Locate and identify every blood parasite.
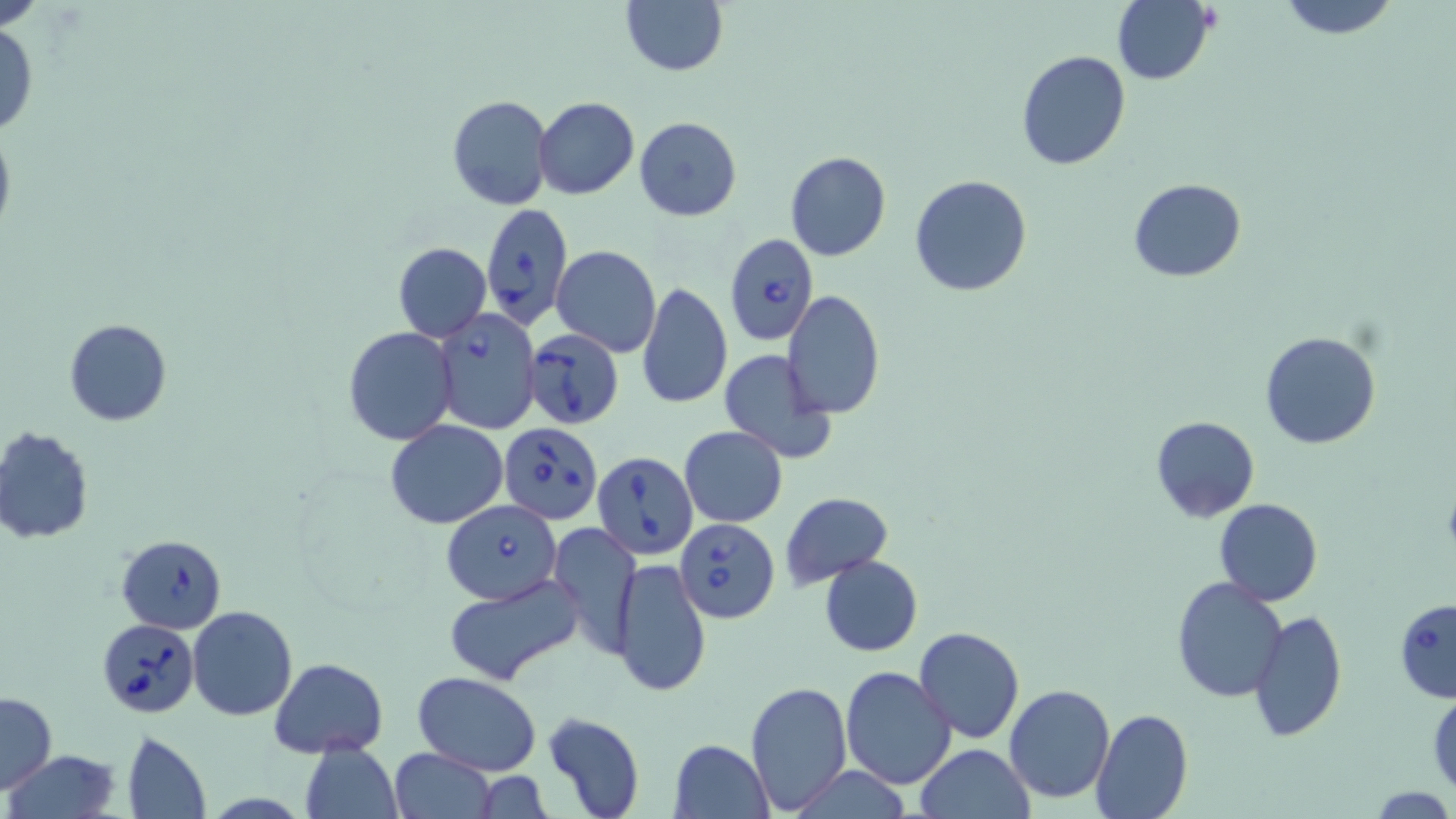
Approximate bounding boxes as named x1/y1/x2/y2 corners in pixels.
Babesia divergens-infected red blood cells: (x1=480, y1=202, x2=572, y2=331), (x1=724, y1=232, x2=816, y2=347), (x1=431, y1=308, x2=541, y2=433), (x1=522, y1=328, x2=625, y2=430), (x1=499, y1=422, x2=602, y2=525), (x1=592, y1=451, x2=698, y2=559), (x1=443, y1=501, x2=562, y2=602), (x1=675, y1=519, x2=779, y2=622), (x1=117, y1=534, x2=227, y2=633), (x1=1395, y1=598, x2=1456, y2=703), (x1=98, y1=617, x2=198, y2=717).
No Plasmodium falciparum, Plasmodium ovale, Plasmodium malariae, Plasmodium vivax, or Trypanosoma brucei observed.

Summary:
  - Uninfected red blood cell locations: (x1=620, y1=0, x2=728, y2=76), (x1=1113, y1=0, x2=1215, y2=85), (x1=1273, y1=0, x2=1404, y2=39), (x1=0, y1=19, x2=40, y2=138), (x1=1015, y1=49, x2=1132, y2=171), (x1=447, y1=94, x2=552, y2=210), (x1=535, y1=97, x2=639, y2=200), (x1=633, y1=116, x2=742, y2=221), (x1=0, y1=118, x2=17, y2=243), (x1=785, y1=151, x2=891, y2=261), (x1=908, y1=173, x2=1034, y2=297), (x1=1128, y1=178, x2=1245, y2=283), (x1=391, y1=242, x2=491, y2=343), (x1=553, y1=246, x2=661, y2=358), (x1=637, y1=284, x2=733, y2=409), (x1=782, y1=290, x2=886, y2=420), (x1=64, y1=319, x2=172, y2=425), (x1=343, y1=327, x2=456, y2=446), (x1=1259, y1=330, x2=1382, y2=449), (x1=717, y1=350, x2=837, y2=464), (x1=1150, y1=415, x2=1260, y2=522), (x1=386, y1=418, x2=509, y2=529), (x1=680, y1=425, x2=787, y2=528), (x1=0, y1=427, x2=94, y2=545), (x1=781, y1=492, x2=892, y2=587), (x1=1214, y1=498, x2=1322, y2=605), (x1=549, y1=522, x2=639, y2=660), (x1=818, y1=554, x2=923, y2=656), (x1=611, y1=558, x2=712, y2=697), (x1=442, y1=573, x2=589, y2=686), (x1=1172, y1=577, x2=1287, y2=701), (x1=187, y1=605, x2=297, y2=721), (x1=1250, y1=609, x2=1348, y2=741), (x1=913, y1=626, x2=1025, y2=744), (x1=269, y1=657, x2=388, y2=758), (x1=840, y1=666, x2=956, y2=791), (x1=412, y1=672, x2=542, y2=776), (x1=743, y1=679, x2=852, y2=814), (x1=1005, y1=683, x2=1116, y2=803), (x1=1428, y1=690, x2=1456, y2=800), (x1=1, y1=693, x2=56, y2=791), (x1=1090, y1=708, x2=1193, y2=819), (x1=542, y1=710, x2=646, y2=819), (x1=120, y1=730, x2=211, y2=818), (x1=669, y1=739, x2=773, y2=818), (x1=298, y1=743, x2=402, y2=819), (x1=916, y1=744, x2=1035, y2=819), (x1=389, y1=748, x2=496, y2=819), (x1=4, y1=749, x2=120, y2=819), (x1=785, y1=765, x2=916, y2=818), (x1=470, y1=774, x2=557, y2=817)
  - Slide-level diagnosis: Babesia divergens
  - Preparation: thin blood film
  - Field of view: single
  - Magnification: 1000x
  - Image size: 1456×819 pixels
  - Modality: optical microscopy
  - Stain: May-Grünwald-Giemsa